Identify the cell.
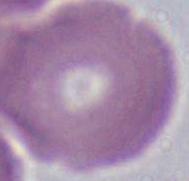
An erythrocyte.

Micrograph. Captured at 1000x magnification.